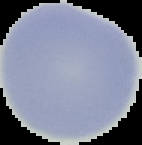
Summary:
  - Image type: segmented cell region with the area outside set to black
  - Preparation: thin blood smear
  - Malaria status: uninfected
  - Image size: 142×145 pixels